Outline each blood parasite and name the species.
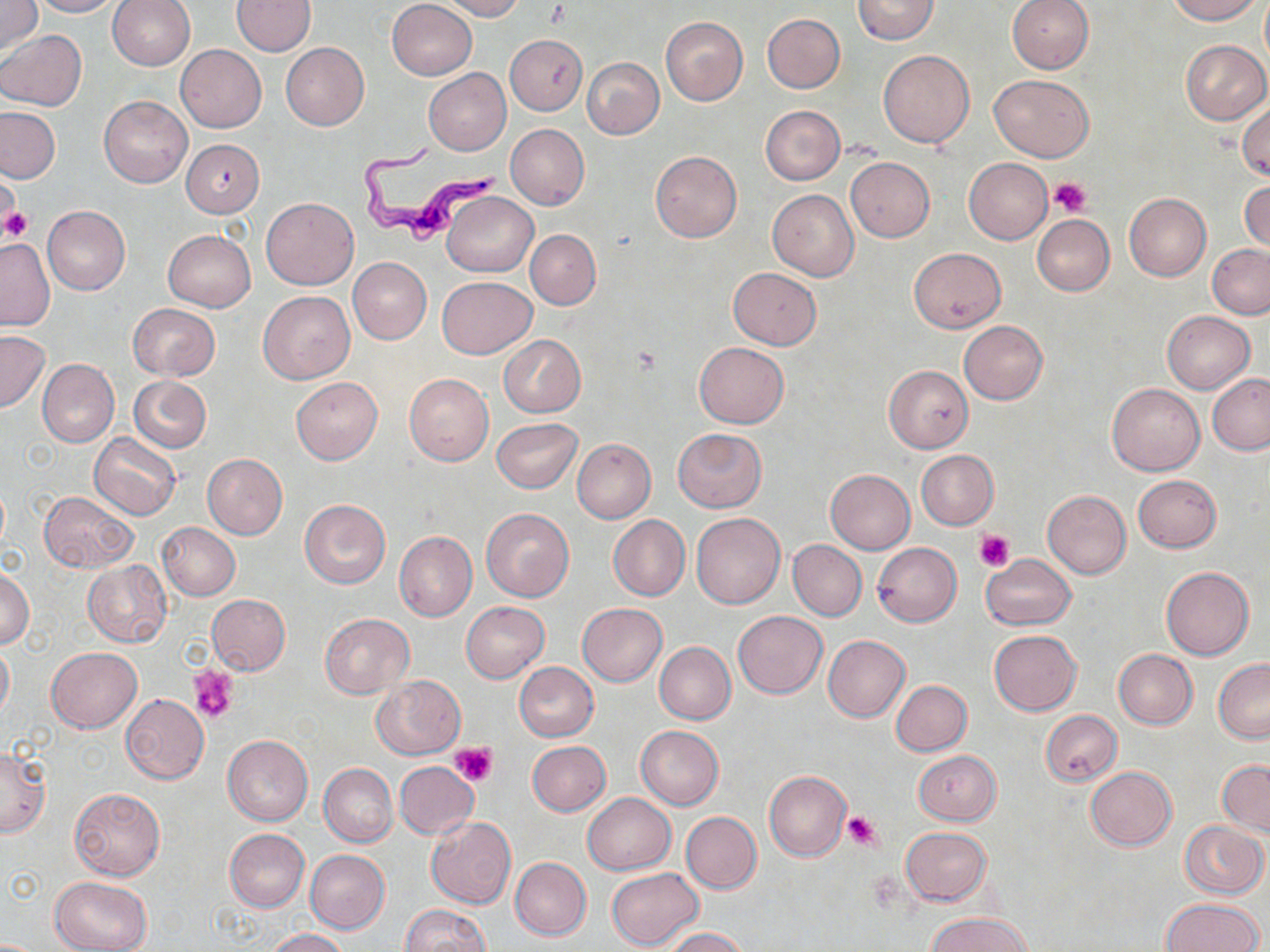
Approximate bounding boxes as [x1, y1, x2, y2] in pixels.
Trypanosoma brucei: [361, 140, 507, 251].
No Plasmodium falciparum, Plasmodium ovale, Plasmodium malariae, Plasmodium vivax, or Babesia divergens observed.

slide-level diagnosis = Trypanosoma brucei
uninfected red blood cell locations = approximate bounding boxes as [x1, y1, x2, y2] in pixels: [0, 0, 42, 56], [28, 0, 120, 17], [107, 0, 195, 69], [233, 0, 316, 55], [387, 0, 476, 80], [440, 0, 524, 20], [851, 0, 938, 45], [1007, 0, 1093, 73], [1166, 0, 1263, 24], [763, 13, 845, 93], [660, 16, 748, 106], [0, 29, 87, 111], [505, 35, 587, 115], [1181, 40, 1269, 124], [281, 42, 369, 130], [175, 45, 266, 132], [878, 50, 974, 148], [582, 57, 664, 138], [423, 68, 511, 155], [989, 74, 1094, 162], [100, 96, 192, 187], [1236, 97, 1270, 182], [760, 106, 846, 184], [0, 107, 59, 183], [505, 124, 589, 210], [181, 139, 265, 217], [650, 151, 742, 242], [846, 157, 935, 242], [963, 157, 1053, 245], [0, 176, 22, 239], [1240, 180, 1269, 256], [768, 189, 859, 280], [442, 191, 537, 277], [1123, 193, 1211, 282], [262, 197, 358, 288], [42, 205, 131, 294], [1032, 215, 1115, 295], [164, 230, 255, 311], [526, 230, 600, 309], [0, 238, 54, 330], [1207, 244, 1270, 318], [908, 248, 1005, 332], [348, 257, 432, 345], [728, 267, 821, 349], [437, 276, 537, 359], [259, 291, 355, 383], [127, 303, 221, 380], [1162, 311, 1254, 394], [959, 321, 1048, 404], [0, 331, 49, 413], [499, 334, 587, 417], [694, 342, 789, 428], [37, 359, 119, 448], [883, 365, 974, 452], [403, 373, 494, 466], [1207, 374, 1270, 455], [129, 376, 211, 453], [291, 377, 383, 465], [1107, 383, 1204, 476], [492, 417, 582, 493], [673, 428, 766, 512], [89, 434, 180, 520], [572, 438, 656, 522], [916, 450, 999, 529], [203, 454, 287, 538], [825, 469, 914, 553], [1133, 474, 1222, 553], [1042, 490, 1131, 578], [39, 491, 137, 572], [300, 500, 390, 588], [481, 508, 574, 602], [691, 513, 785, 607], [609, 515, 690, 600], [157, 522, 241, 600], [394, 531, 476, 621], [788, 540, 867, 620], [873, 542, 961, 626], [978, 554, 1077, 630], [83, 561, 171, 646], [1, 566, 34, 651], [1162, 567, 1254, 660], [207, 594, 290, 675], [461, 602, 549, 683], [578, 603, 667, 687], [733, 611, 828, 699], [320, 613, 415, 699], [989, 629, 1082, 716], [823, 635, 910, 721], [0, 642, 13, 722], [655, 642, 735, 724], [45, 647, 142, 733], [1113, 650, 1197, 729], [1213, 659, 1270, 743], [514, 661, 598, 741], [372, 675, 465, 759], [891, 680, 972, 756], [120, 693, 209, 783], [1040, 709, 1122, 786], [636, 725, 723, 809], [223, 735, 313, 825], [527, 740, 610, 816], [0, 747, 50, 837], [913, 750, 1001, 825], [1217, 760, 1270, 837], [394, 761, 478, 839], [319, 763, 397, 846], [1085, 766, 1176, 851], [763, 771, 850, 860], [69, 788, 165, 881], [583, 793, 675, 874], [680, 812, 762, 893], [426, 818, 516, 909], [1179, 821, 1268, 898], [901, 827, 991, 906], [224, 829, 309, 911], [305, 849, 389, 934], [510, 858, 591, 940], [607, 868, 703, 950], [50, 876, 152, 952], [1162, 898, 1263, 951], [400, 904, 491, 952], [928, 912, 1033, 952], [664, 927, 748, 952], [265, 928, 349, 951]
stain = May-Grünwald-Giemsa
magnification = 1000x
platelet locations = approximate bounding boxes as [x1, y1, x2, y2] in pixels: [1048, 177, 1091, 217], [2, 206, 32, 244], [975, 529, 1015, 571], [189, 664, 239, 723], [450, 743, 497, 786], [842, 812, 883, 851]
image size = 1270×952 pixels
preparation = thin blood film
modality = optical microscopy
field of view = single